Locate every Plasmodium falciparum parasite and identify its life-cycle stage.
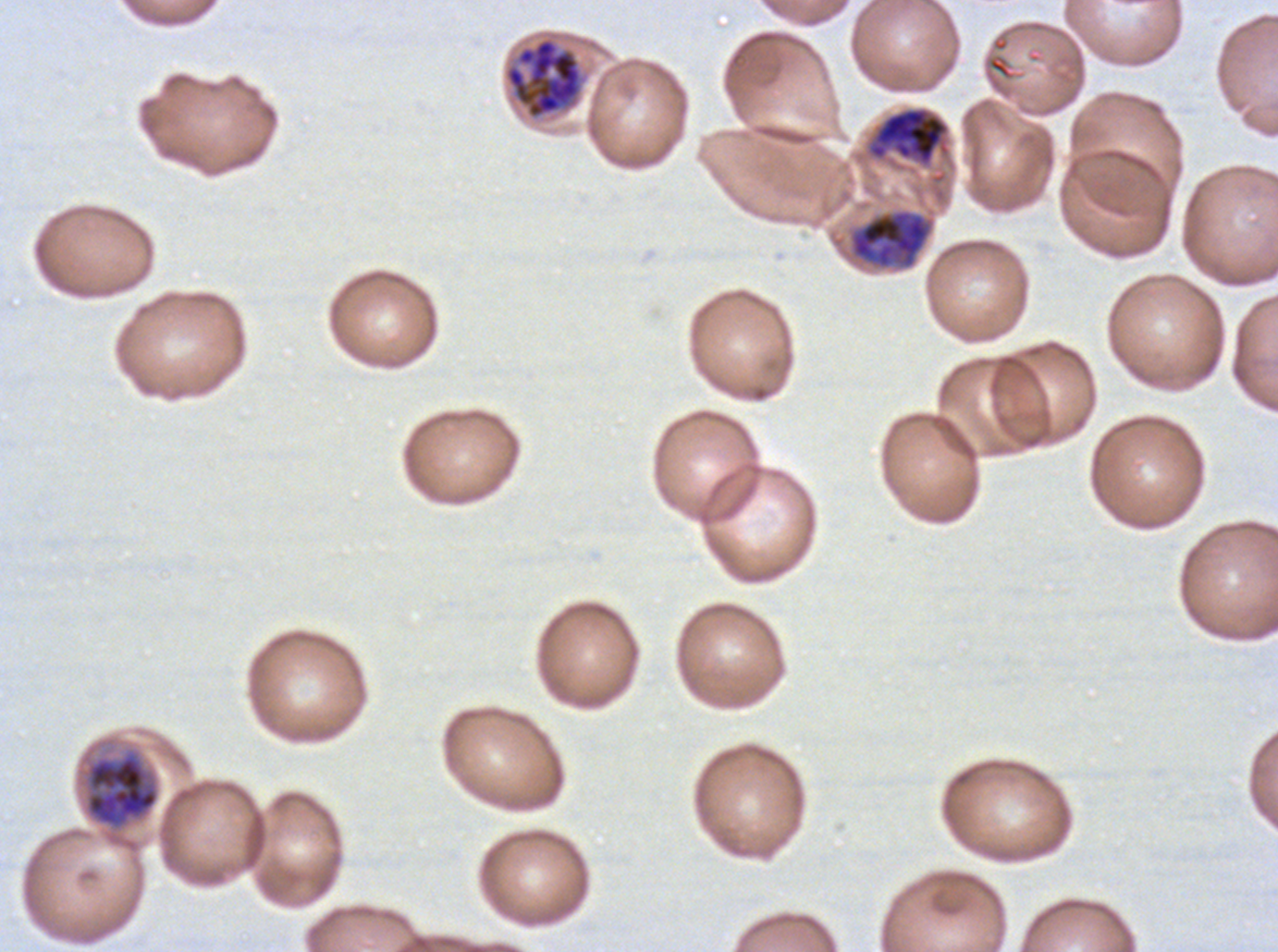

Approximate bounding rectangles given as corner coordinates in pixels from the top-left.
Late trophozoites: (x1=848, y1=208, x2=935, y2=270).
Late schizonts: (x1=503, y1=36, x2=584, y2=120), (x1=866, y1=105, x2=951, y2=168), (x1=80, y1=747, x2=160, y2=832).
No rings, late-ring/early-trophozoite forms, mid trophozoites, early schizonts, segmenters, or gametocytes observed.

Summary:
  - Preparation: thin blood smear
  - Stain: Giemsa
  - Image size: 1278×952 pixels
  - Field of view: one sub-image of a larger composite
  - Specimen: ex-vivo Plasmodium falciparum culture from a patient in The Gambia, grown for 24 to 48 hours
  - Life-cycle stages observed: late trophozoite, late schizont